Assess the morphology of the red blood cells.
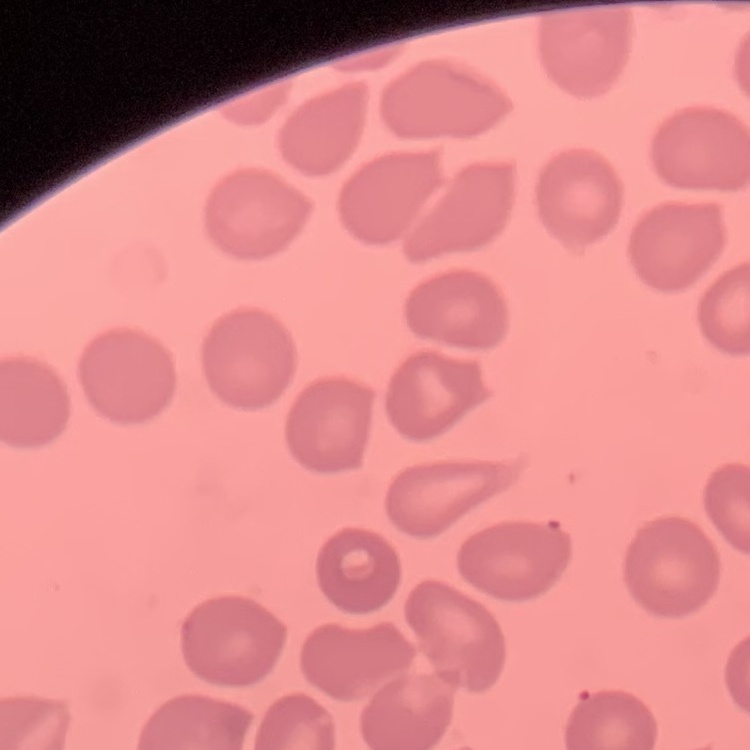

No rouleaux formation.

Stained with either Field's or Giemsa. One tile cut from a larger photomicrograph. Thin blood film.